Locate every Plasmodium parasite and every leukocyte.
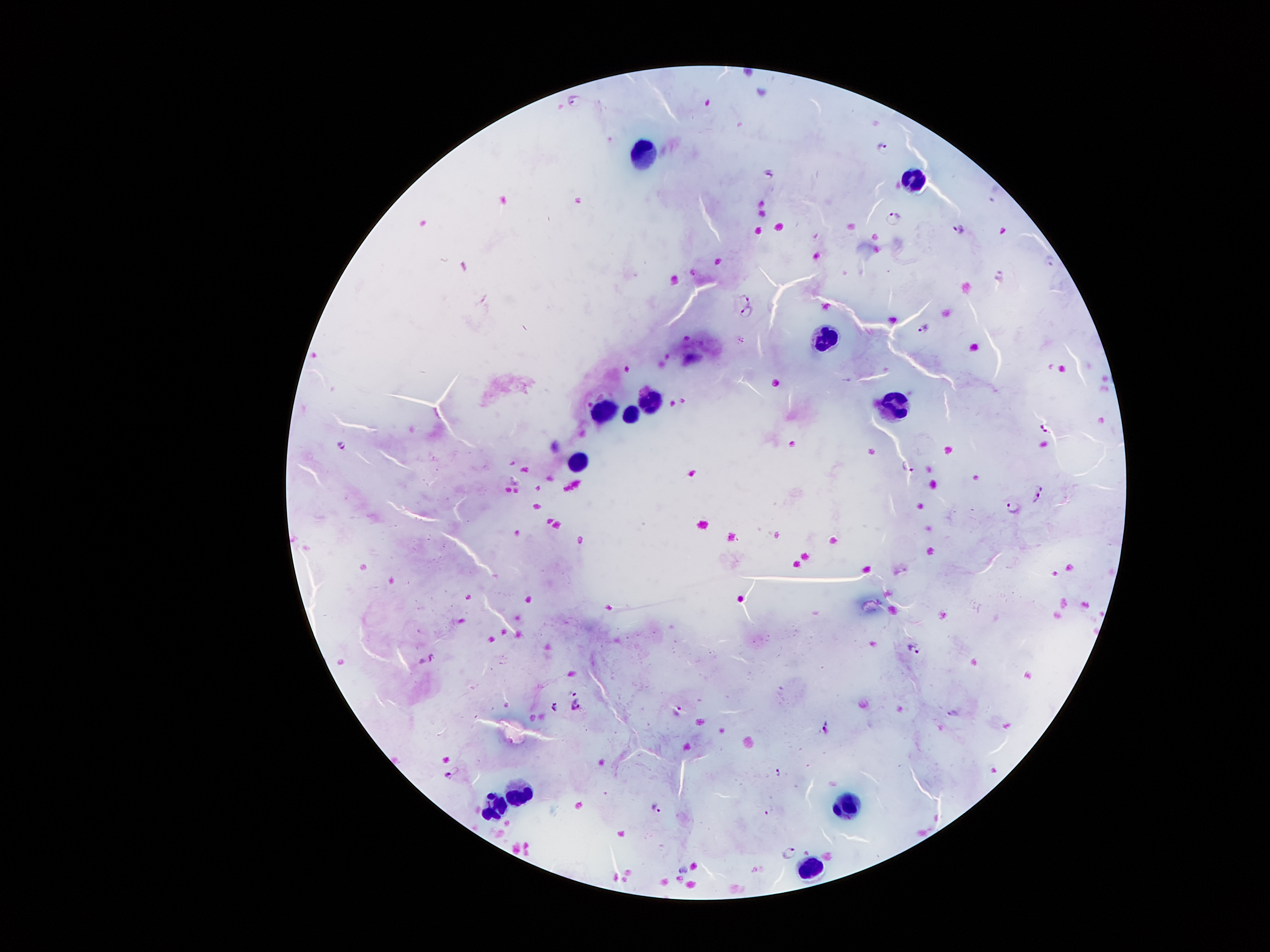
Approximate centers as {x, y} in pixels.
Plasmodium parasites: {575, 99}, {884, 146}, {771, 172}, {892, 217}, {959, 229}, {1051, 260}, {745, 299}, {746, 312}, {922, 328}, {1044, 428}, {341, 444}, {908, 465}, {1040, 487}, {1036, 498}, {1012, 508}, {912, 649}, {433, 657}, {573, 694}, {575, 706}, {554, 707}, {678, 710}, {954, 715}, {824, 729}, {777, 771}, {449, 774}, {656, 809}, {789, 852}, {683, 869}.
Leukocytes: {649, 152}, {914, 179}, {827, 338}, {651, 399}, {891, 405}, {604, 409}, {631, 414}, {578, 462}, {519, 792}, {848, 807}, {493, 809}, {808, 870}.

Thick blood smear. Patient malaria status: positive for Plasmodium falciparum. One field from this slide. Photographed through the microscope eyepiece with a smartphone camera. Giemsa-stained preparation. 100x magnification. Image is 1270×952 pixels.